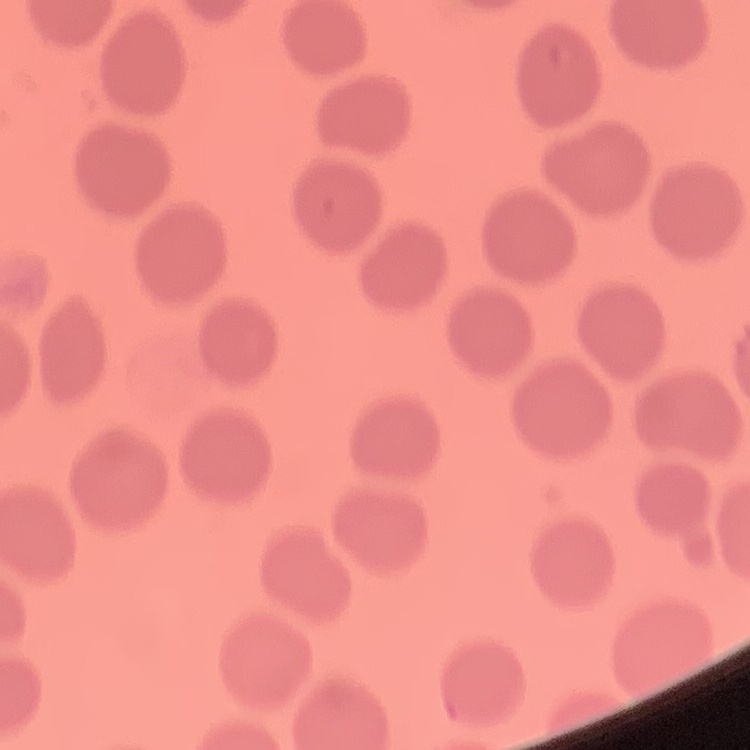
The red blood cells exhibit no rouleaux formation. Field's or Giemsa stain. Thin blood film. Square crop of a larger photomicrograph.